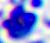
identification: white blood cell
modality: micrograph
magnification: 400x